Give the extent of all white blood cells.
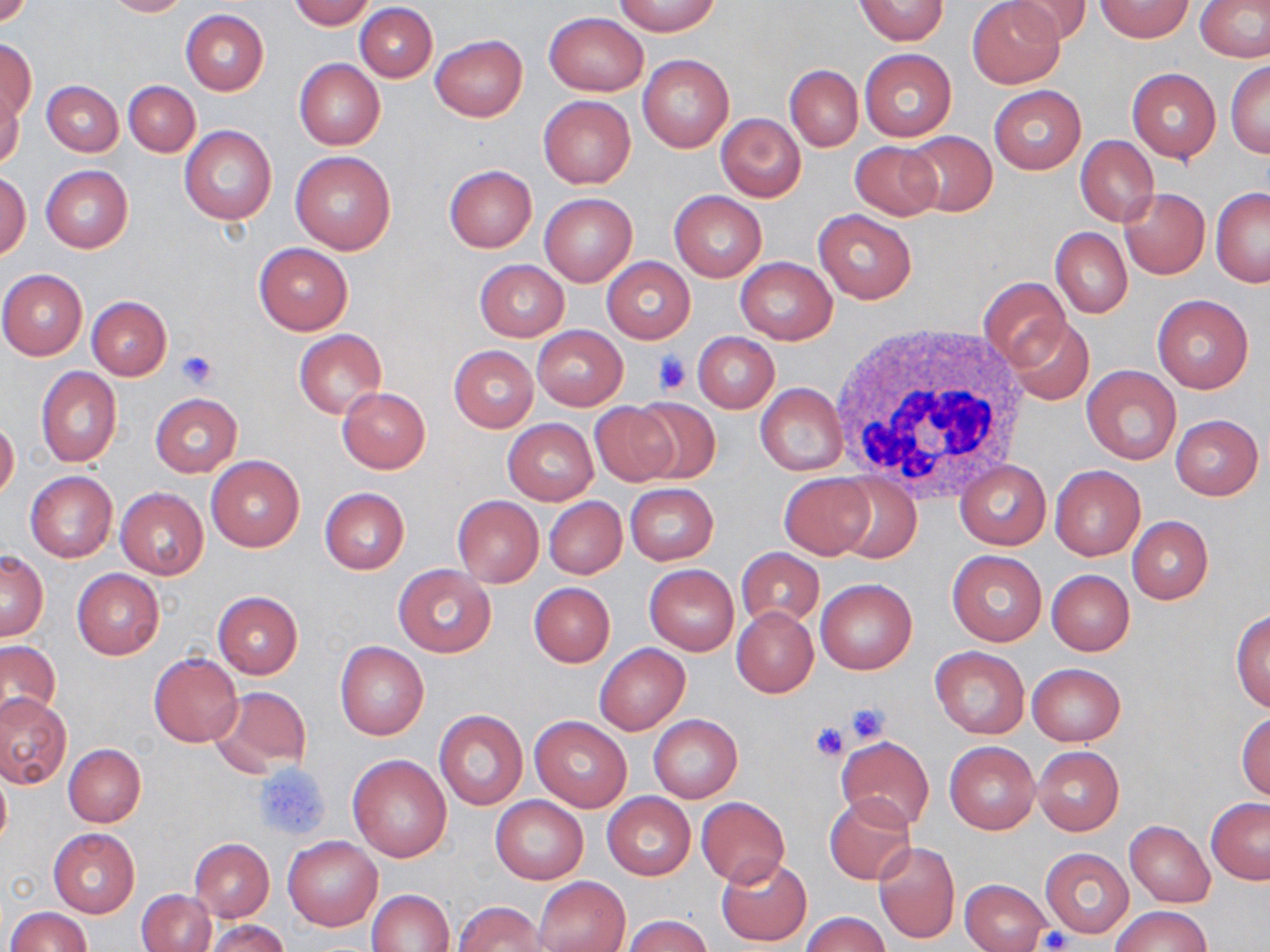
Approximate bounding boxes as named x1/y1/x2/y2 corners in pixels.
White blood cells: (x1=829, y1=322, x2=1033, y2=503).

Summary:
  - Platelet locations: (x1=175, y1=351, x2=217, y2=389), (x1=651, y1=352, x2=694, y2=393), (x1=844, y1=702, x2=890, y2=746), (x1=810, y1=722, x2=849, y2=762), (x1=253, y1=761, x2=331, y2=841), (x1=1040, y1=927, x2=1072, y2=951)
  - Uninfected red blood cell locations: (x1=103, y1=0, x2=189, y2=17), (x1=288, y1=0, x2=375, y2=29), (x1=855, y1=0, x2=948, y2=46), (x1=1007, y1=0, x2=1092, y2=45), (x1=1096, y1=0, x2=1192, y2=42), (x1=0, y1=1, x2=34, y2=30), (x1=615, y1=1, x2=720, y2=36), (x1=967, y1=1, x2=1064, y2=87), (x1=1196, y1=1, x2=1270, y2=63), (x1=355, y1=4, x2=437, y2=83), (x1=181, y1=10, x2=268, y2=94), (x1=543, y1=11, x2=649, y2=96), (x1=431, y1=34, x2=527, y2=122), (x1=0, y1=38, x2=36, y2=122), (x1=859, y1=49, x2=957, y2=140), (x1=638, y1=54, x2=733, y2=153), (x1=294, y1=59, x2=384, y2=149), (x1=1226, y1=61, x2=1270, y2=157), (x1=785, y1=65, x2=862, y2=151), (x1=1127, y1=67, x2=1221, y2=162), (x1=123, y1=80, x2=201, y2=156), (x1=42, y1=81, x2=123, y2=156), (x1=989, y1=86, x2=1086, y2=174), (x1=1, y1=91, x2=24, y2=171), (x1=539, y1=95, x2=636, y2=189), (x1=716, y1=113, x2=805, y2=200), (x1=179, y1=126, x2=277, y2=225), (x1=901, y1=131, x2=997, y2=217), (x1=1075, y1=136, x2=1158, y2=226), (x1=849, y1=142, x2=940, y2=220), (x1=290, y1=151, x2=396, y2=254), (x1=444, y1=164, x2=537, y2=252), (x1=41, y1=165, x2=133, y2=253), (x1=1, y1=170, x2=31, y2=259), (x1=1210, y1=187, x2=1270, y2=287), (x1=1119, y1=188, x2=1210, y2=279), (x1=670, y1=190, x2=766, y2=281), (x1=540, y1=193, x2=636, y2=286), (x1=813, y1=209, x2=917, y2=305), (x1=1051, y1=228, x2=1131, y2=318), (x1=254, y1=242, x2=353, y2=334), (x1=602, y1=257, x2=695, y2=343), (x1=734, y1=257, x2=838, y2=344), (x1=475, y1=260, x2=569, y2=341), (x1=0, y1=270, x2=87, y2=359), (x1=980, y1=276, x2=1070, y2=368), (x1=1151, y1=295, x2=1254, y2=393), (x1=87, y1=297, x2=171, y2=380), (x1=1006, y1=317, x2=1094, y2=405), (x1=533, y1=326, x2=627, y2=410), (x1=293, y1=330, x2=387, y2=418), (x1=693, y1=332, x2=779, y2=412), (x1=448, y1=345, x2=538, y2=432), (x1=1082, y1=365, x2=1182, y2=464), (x1=36, y1=367, x2=121, y2=466), (x1=755, y1=384, x2=848, y2=477), (x1=337, y1=387, x2=430, y2=473), (x1=150, y1=393, x2=241, y2=477), (x1=629, y1=396, x2=721, y2=484), (x1=588, y1=402, x2=679, y2=486), (x1=1170, y1=415, x2=1264, y2=500), (x1=0, y1=417, x2=19, y2=501), (x1=503, y1=419, x2=598, y2=505), (x1=206, y1=456, x2=305, y2=551), (x1=956, y1=461, x2=1051, y2=549), (x1=1050, y1=464, x2=1145, y2=560), (x1=24, y1=470, x2=117, y2=563), (x1=780, y1=474, x2=874, y2=558), (x1=831, y1=475, x2=922, y2=561), (x1=625, y1=483, x2=718, y2=565), (x1=319, y1=487, x2=410, y2=574), (x1=116, y1=488, x2=208, y2=579), (x1=452, y1=495, x2=543, y2=587), (x1=544, y1=497, x2=626, y2=579), (x1=1127, y1=516, x2=1212, y2=604), (x1=737, y1=547, x2=824, y2=629), (x1=947, y1=550, x2=1047, y2=646), (x1=0, y1=551, x2=48, y2=641), (x1=393, y1=564, x2=496, y2=657), (x1=644, y1=564, x2=739, y2=655), (x1=71, y1=569, x2=164, y2=659), (x1=1046, y1=569, x2=1135, y2=655), (x1=815, y1=578, x2=916, y2=674), (x1=528, y1=583, x2=615, y2=667), (x1=213, y1=591, x2=302, y2=679), (x1=732, y1=607, x2=818, y2=697), (x1=1232, y1=609, x2=1270, y2=713), (x1=0, y1=640, x2=61, y2=723), (x1=336, y1=642, x2=429, y2=740), (x1=595, y1=643, x2=690, y2=734), (x1=929, y1=646, x2=1029, y2=739), (x1=149, y1=654, x2=242, y2=748), (x1=1027, y1=662, x2=1125, y2=746), (x1=212, y1=686, x2=312, y2=774), (x1=0, y1=693, x2=70, y2=787), (x1=434, y1=710, x2=528, y2=809), (x1=1237, y1=711, x2=1270, y2=801), (x1=648, y1=714, x2=743, y2=802), (x1=528, y1=716, x2=632, y2=812), (x1=836, y1=736, x2=935, y2=831), (x1=943, y1=741, x2=1040, y2=834), (x1=64, y1=743, x2=146, y2=826), (x1=1033, y1=746, x2=1124, y2=835), (x1=348, y1=754, x2=453, y2=862), (x1=0, y1=767, x2=11, y2=851), (x1=602, y1=792, x2=696, y2=880), (x1=824, y1=795, x2=916, y2=885), (x1=491, y1=796, x2=588, y2=884), (x1=696, y1=797, x2=790, y2=886), (x1=1206, y1=797, x2=1270, y2=884), (x1=1124, y1=820, x2=1215, y2=907), (x1=49, y1=829, x2=139, y2=916), (x1=283, y1=836, x2=382, y2=931), (x1=189, y1=838, x2=274, y2=922), (x1=873, y1=842, x2=959, y2=943), (x1=1040, y1=846, x2=1134, y2=938), (x1=716, y1=857, x2=812, y2=945), (x1=535, y1=878, x2=629, y2=952), (x1=960, y1=879, x2=1050, y2=952), (x1=368, y1=888, x2=455, y2=952), (x1=138, y1=889, x2=216, y2=952), (x1=455, y1=901, x2=549, y2=952), (x1=1111, y1=905, x2=1211, y2=952), (x1=5, y1=907, x2=91, y2=952), (x1=801, y1=912, x2=889, y2=952), (x1=624, y1=914, x2=712, y2=952), (x1=204, y1=919, x2=288, y2=952)
  - Slide-level diagnosis: no evidence of blood parasites
  - Preparation: thin blood film
  - Modality: light microscopy
  - Magnification: 1000x
  - Stain: May-Grünwald-Giemsa
  - Field of view: single
  - Image size: 1270×952 pixels